Assess the morphology of the red blood cells.
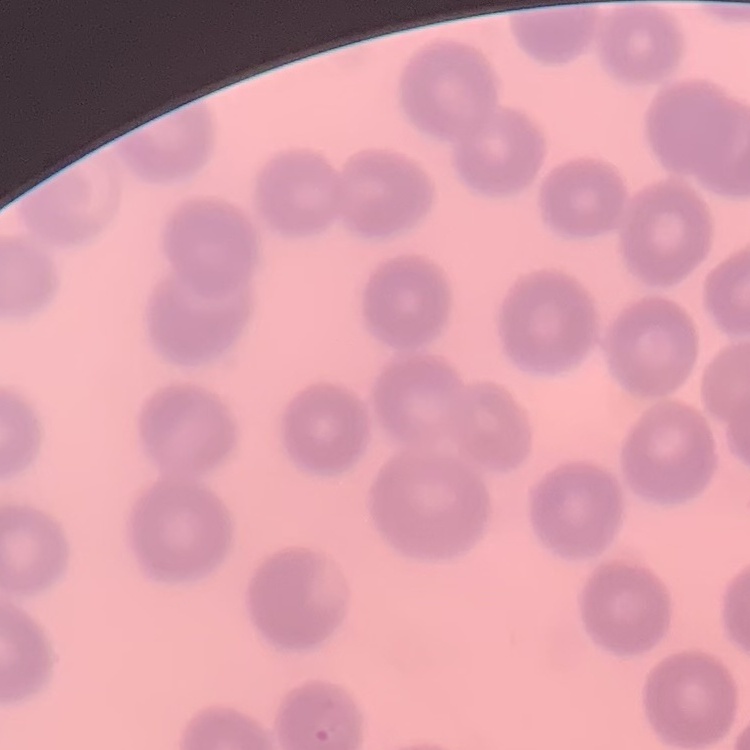
They show no rouleaux formation.

Summary:
  - Image type: square crop of a larger photomicrograph
  - Stain: Field's or Giemsa
  - Preparation: thin blood film